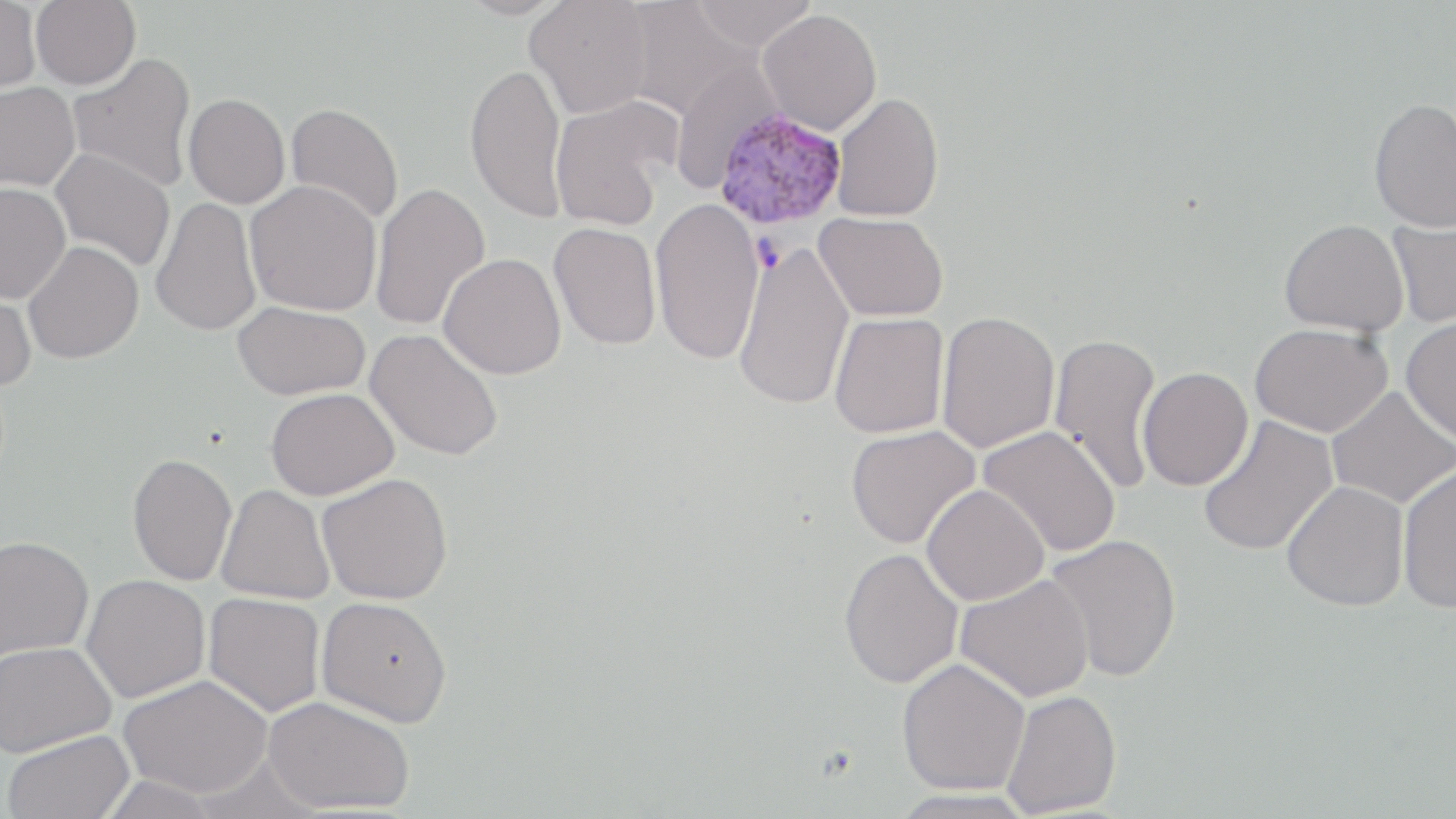
Summary:
  - Coordinate format: approximate bounding boxes as named x1/y1/x2/y2 corners in pixels
  - Uninfected red blood cell locations: (x1=0, y1=0, x2=42, y2=94), (x1=31, y1=0, x2=141, y2=89), (x1=455, y1=0, x2=572, y2=20), (x1=525, y1=0, x2=653, y2=119), (x1=692, y1=0, x2=818, y2=51), (x1=618, y1=1, x2=752, y2=121), (x1=757, y1=9, x2=882, y2=135), (x1=67, y1=53, x2=198, y2=192), (x1=669, y1=60, x2=785, y2=194), (x1=465, y1=63, x2=569, y2=223), (x1=0, y1=82, x2=81, y2=191), (x1=831, y1=92, x2=944, y2=222), (x1=184, y1=93, x2=290, y2=208), (x1=550, y1=95, x2=680, y2=230), (x1=1369, y1=97, x2=1456, y2=232), (x1=286, y1=102, x2=404, y2=226), (x1=50, y1=148, x2=176, y2=272), (x1=246, y1=180, x2=382, y2=316), (x1=370, y1=181, x2=490, y2=332), (x1=0, y1=182, x2=70, y2=303), (x1=650, y1=197, x2=765, y2=365), (x1=150, y1=198, x2=261, y2=337), (x1=814, y1=211, x2=948, y2=322), (x1=1387, y1=216, x2=1456, y2=329), (x1=1279, y1=219, x2=1409, y2=336), (x1=549, y1=222, x2=661, y2=351), (x1=733, y1=239, x2=855, y2=411), (x1=23, y1=241, x2=144, y2=364), (x1=439, y1=253, x2=566, y2=379), (x1=0, y1=281, x2=37, y2=391), (x1=233, y1=301, x2=371, y2=400), (x1=936, y1=310, x2=1060, y2=453), (x1=829, y1=312, x2=949, y2=439), (x1=1401, y1=315, x2=1456, y2=444), (x1=1250, y1=322, x2=1392, y2=437), (x1=365, y1=328, x2=503, y2=461), (x1=1049, y1=331, x2=1163, y2=494), (x1=1137, y1=366, x2=1253, y2=491), (x1=1327, y1=386, x2=1456, y2=509), (x1=266, y1=387, x2=399, y2=500), (x1=1197, y1=414, x2=1338, y2=558), (x1=845, y1=425, x2=980, y2=549), (x1=977, y1=426, x2=1120, y2=557), (x1=127, y1=452, x2=237, y2=586), (x1=1396, y1=464, x2=1456, y2=613), (x1=317, y1=472, x2=453, y2=604), (x1=1282, y1=480, x2=1410, y2=611), (x1=921, y1=484, x2=1049, y2=605), (x1=216, y1=485, x2=335, y2=604), (x1=1043, y1=534, x2=1183, y2=683), (x1=0, y1=535, x2=94, y2=662), (x1=838, y1=548, x2=964, y2=688), (x1=81, y1=574, x2=211, y2=703), (x1=955, y1=574, x2=1094, y2=702), (x1=204, y1=592, x2=326, y2=717), (x1=316, y1=596, x2=453, y2=727), (x1=0, y1=641, x2=115, y2=756), (x1=897, y1=658, x2=1030, y2=795), (x1=119, y1=675, x2=273, y2=797), (x1=1001, y1=689, x2=1122, y2=817), (x1=263, y1=696, x2=415, y2=815), (x1=3, y1=730, x2=135, y2=819), (x1=890, y1=788, x2=1040, y2=818)
  - Plasmodium vivax-infected red blood cell locations: (x1=712, y1=108, x2=847, y2=231)
  - Slide-level diagnosis: Plasmodium vivax
  - Magnification: 1000x
  - Preparation: thin blood film
  - Stain: May-Grünwald-Giemsa
  - Field of view: one of a larger specimen
  - Image size: 1456×819 pixels
  - Modality: optical microscopy